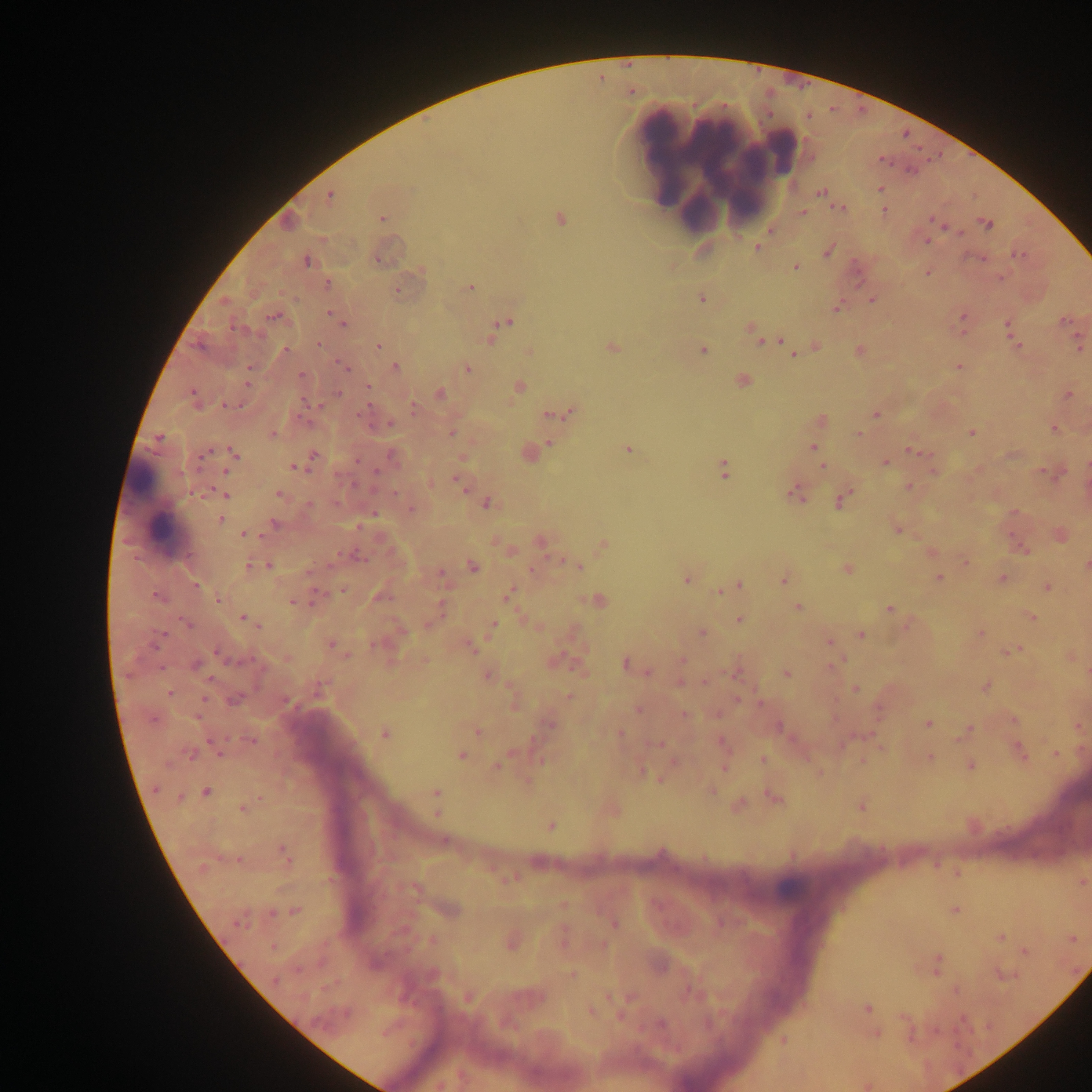

field of view = single
leukocyte locations = approximate centers as {x, y} in pixels: {659, 154}, {718, 165}, {154, 505}, {788, 887}
country = Ghana
malaria parasite locations = approximate centers as {x, y} in pixels: {882, 160}, {881, 189}, {821, 192}, {330, 196}, {840, 209}, {885, 211}, {802, 213}, {383, 218}, {560, 219}, {933, 220}, {987, 224}, {960, 233}, {927, 241}, {757, 248}, {829, 251}, {1019, 255}, {977, 259}, {377, 260}, {306, 261}, {795, 267}, {927, 273}, {1001, 279}, {328, 283}, {471, 288}, {398, 291}, {702, 299}, {872, 300}, {837, 307}, {332, 315}, {963, 315}, {276, 317}, {1065, 321}, {342, 323}, {505, 323}, {497, 327}, {1008, 327}, {753, 331}, {757, 337}, {1012, 338}, {490, 339}, {772, 340}, {782, 340}, {1015, 344}, {319, 345}, {379, 346}, {612, 347}, {817, 347}, {1080, 347}, {286, 350}, {703, 350}, {859, 351}, {794, 355}, {395, 367}, {959, 367}, {345, 368}, {468, 368}, {249, 369}, {301, 375}, {742, 380}, {519, 387}, {369, 388}, {440, 393}, {192, 394}, {337, 394}, {1069, 395}, {231, 405}, {413, 407}, {572, 412}, {362, 414}, {877, 414}, {548, 416}, {821, 420}, {390, 423}, {1054, 429}, {971, 432}, {452, 433}, {858, 434}, {273, 435}, {159, 438}, {549, 443}, {813, 447}, {628, 450}, {912, 451}, {234, 453}, {313, 455}, {392, 456}, {885, 463}, {822, 466}, {294, 467}, {724, 468}, {225, 471}, {376, 471}, {934, 471}, {457, 480}, {909, 486}, {395, 493}, {224, 494}, {279, 494}, {796, 494}, {842, 500}, {487, 504}, {309, 505}, {411, 510}, {373, 513}, {1014, 513}, {221, 519}, {275, 524}, {898, 529}, {244, 534}, {541, 541}, {602, 545}, {1023, 550}, {932, 551}, {966, 562}, {1086, 565}, {249, 566}, {270, 566}, {472, 566}, {577, 566}, {848, 569}, {533, 570}, {308, 572}, {440, 573}, {939, 578}, {1003, 579}, {686, 580}, {784, 580}, {196, 585}, {739, 586}, {1047, 587}, {719, 592}, {509, 594}, {158, 597}, {219, 599}, {596, 601}, {292, 602}, {797, 608}, {889, 609}, {1031, 616}, {245, 618}, {739, 619}, {186, 623}, {493, 625}, {701, 633}, {861, 634}, {981, 634}, {157, 641}, {828, 642}, {331, 644}, {469, 646}, {1013, 651}, {219, 655}, {347, 655}, {682, 660}, {555, 661}, {626, 663}, {197, 665}, {835, 665}, {647, 671}, {736, 674}, {787, 674}, {487, 675}, {680, 683}, {705, 683}, {986, 687}, {856, 689}, {169, 694}, {569, 696}, {235, 700}, {737, 700}, {761, 702}, {638, 710}, {685, 714}, {928, 723}, {549, 725}, {779, 726}, {479, 731}, {967, 731}, {620, 733}, {384, 735}, {251, 740}, {722, 742}, {658, 744}, {1020, 752}, {1056, 753}, {191, 754}, {461, 755}, {930, 758}, {763, 759}, {970, 765}, {497, 766}, {724, 769}, {659, 780}, {156, 790}, {207, 792}, {436, 792}, {712, 792}, {772, 798}, {739, 805}, {862, 806}, {242, 808}, {437, 813}, {550, 826}, {285, 854}, {507, 879}, {416, 889}, {451, 909}, {956, 910}, {295, 911}, {271, 914}, {240, 921}, {614, 923}, {1001, 937}, {433, 940}, {512, 942}, {273, 948}, {1026, 951}, {938, 958}, {1005, 974}, {571, 975}, {469, 998}, {868, 1009}, {590, 1011}, {660, 1024}, {876, 1033}, {783, 1040}
capture = mobile-phone photograph through a microscope
preparation = thick blood smear
image size = 1092×1092 pixels